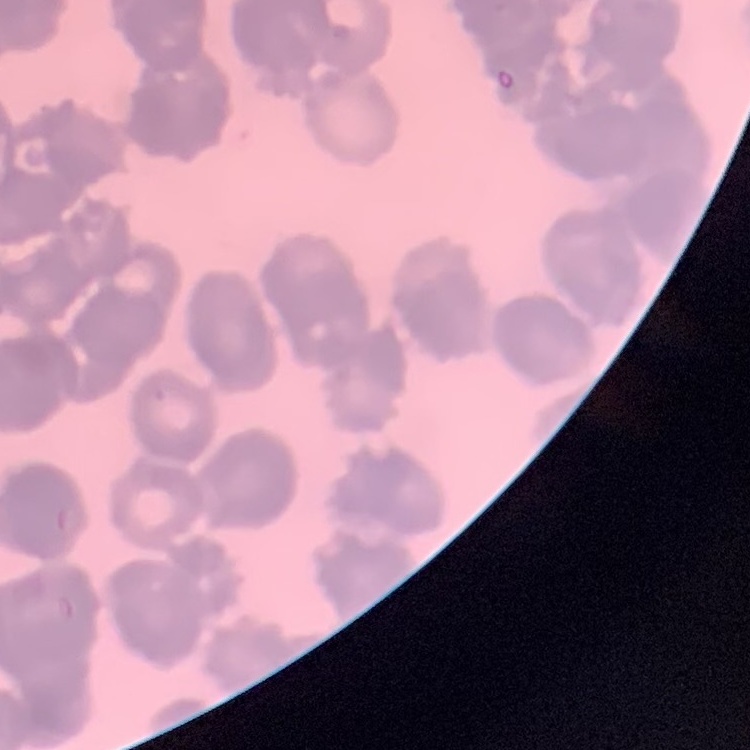
The erythrocytes exhibit rouleaux formation. One tile cut from a larger photomicrograph. Thin peripheral smear. Stained with either Field's or Giemsa.